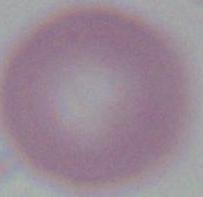

Photomicrograph. An erythrocyte is shown. Captured at 1000x magnification.